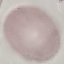

Summary:
  - Malaria status: uninfected
  - Image type: cell patch, automatically extracted from a larger field of view and resized to 64 × 64 pixels
  - Stain: Giemsa
  - Preparation: thin blood film
  - Capture: smartphone camera at the microscope eyepiece